Report the malaria status of this cell.
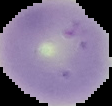
It is uninfected.

image type = cell region segmented out of the field of view; surrounding area masked to black
image size = 112×106 pixels
preparation = thin blood film